Outline each blood parasite and name the species.
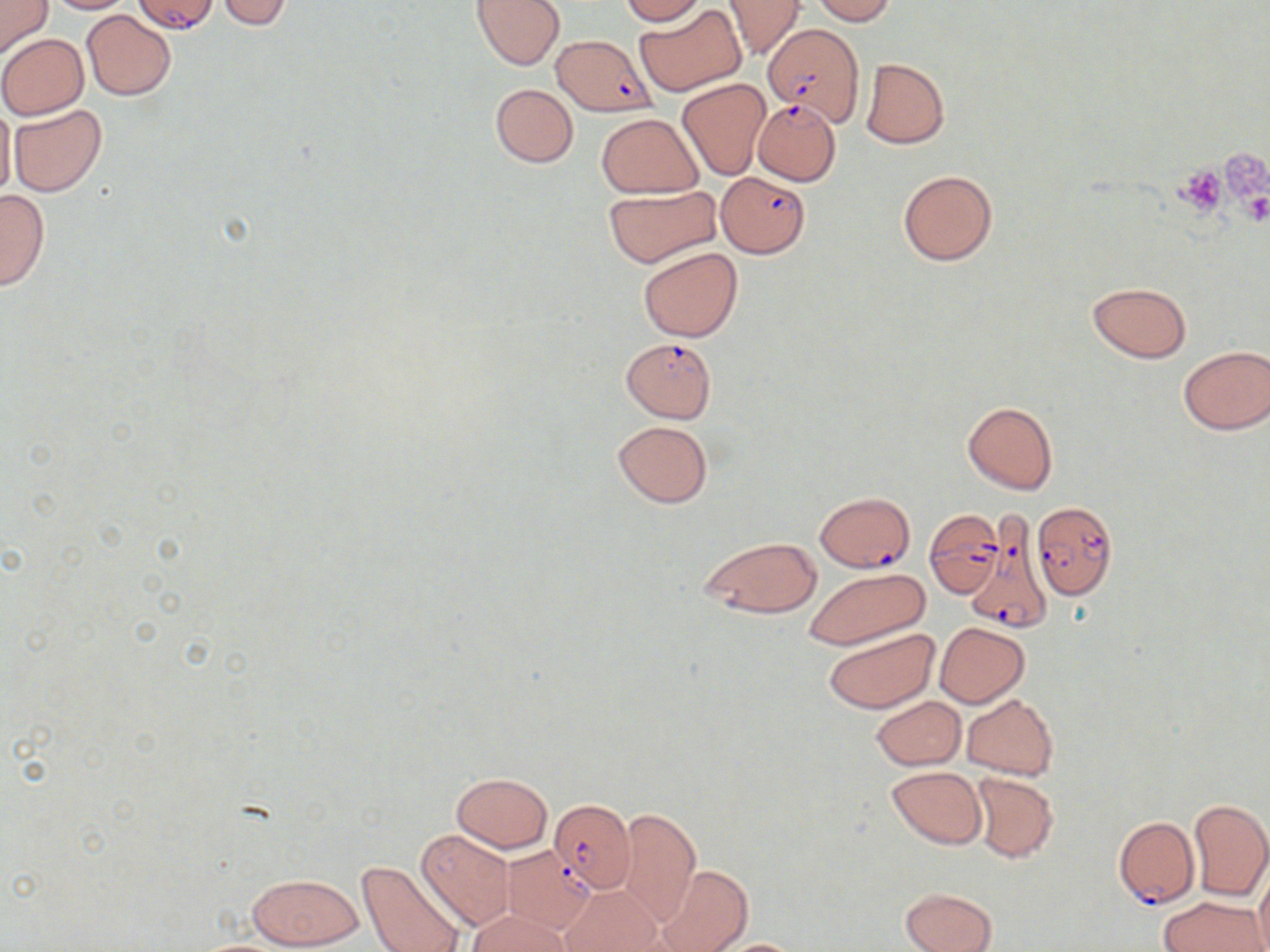
Approximate bounding boxes as (x1,y1)-(x2,y2) corner pairs in pixels.
Plasmodium falciparum-infected red blood cells: (761,25)-(860,123), (551,35)-(657,117), (750,99)-(841,189), (718,170)-(812,257), (620,338)-(717,424), (815,491)-(915,572), (1033,500)-(1118,599), (924,510)-(1003,596), (966,521)-(1051,635), (550,801)-(634,894), (1113,815)-(1199,909).
No Plasmodium ovale, Plasmodium malariae, Plasmodium vivax, Babesia divergens, or Trypanosoma brucei observed.

Platelet locations: (1216,150)-(1270,211), (1174,165)-(1228,214). Uninfected red blood cell locations: (0,0)-(53,58), (43,0)-(135,13), (132,0)-(219,35), (472,0)-(564,69), (618,0)-(707,24), (722,0)-(805,59), (811,0)-(896,24), (216,1)-(295,28), (635,4)-(747,96), (81,9)-(176,100), (0,33)-(89,118), (861,57)-(950,149), (676,79)-(770,180), (490,83)-(579,168), (0,99)-(16,203), (8,104)-(107,197), (597,113)-(701,198), (898,170)-(997,266), (603,185)-(722,268), (0,189)-(50,291), (638,246)-(742,342), (1087,281)-(1191,362), (1178,344)-(1270,434), (963,402)-(1058,495), (611,420)-(713,508), (699,535)-(823,619), (803,565)-(930,651), (934,621)-(1030,707), (822,628)-(939,713), (961,694)-(1059,779), (871,695)-(967,771), (887,767)-(986,848), (970,771)-(1058,864), (452,773)-(553,851), (1188,798)-(1270,902), (616,806)-(700,927), (416,829)-(515,928), (500,846)-(597,934), (355,859)-(465,952), (1254,863)-(1270,951), (655,865)-(752,952), (245,872)-(366,949), (478,876)-(584,950), (562,884)-(662,952), (899,887)-(998,952), (1160,896)-(1266,952), (468,911)-(568,952), (708,938)-(808,951). Slide-level diagnosis: Plasmodium falciparum. One field of a larger specimen. Light microscopy. May-Grünwald-Giemsa stain. Image is 1270×952 pixels. Captured at 1000x magnification. Thin blood film.